Classify this cell by malaria status.
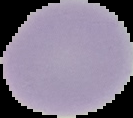
It is uninfected.

Summary:
  - Image type: segmented cell region on a black background
  - Image size: 133×118 pixels
  - Preparation: thin blood film